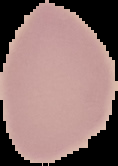

image type = segmented cell region on a black background
preparation = thin blood film
result = negative for Plasmodium parasites
image size = 118×166 pixels